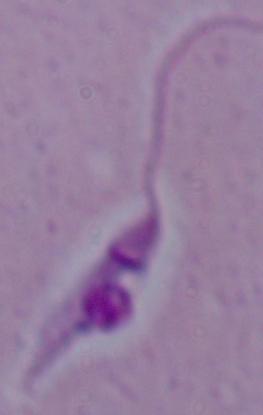
A Leishmania parasite is seen. Photomicrograph. 1000x magnification.